Assess for Plasmodium parasites.
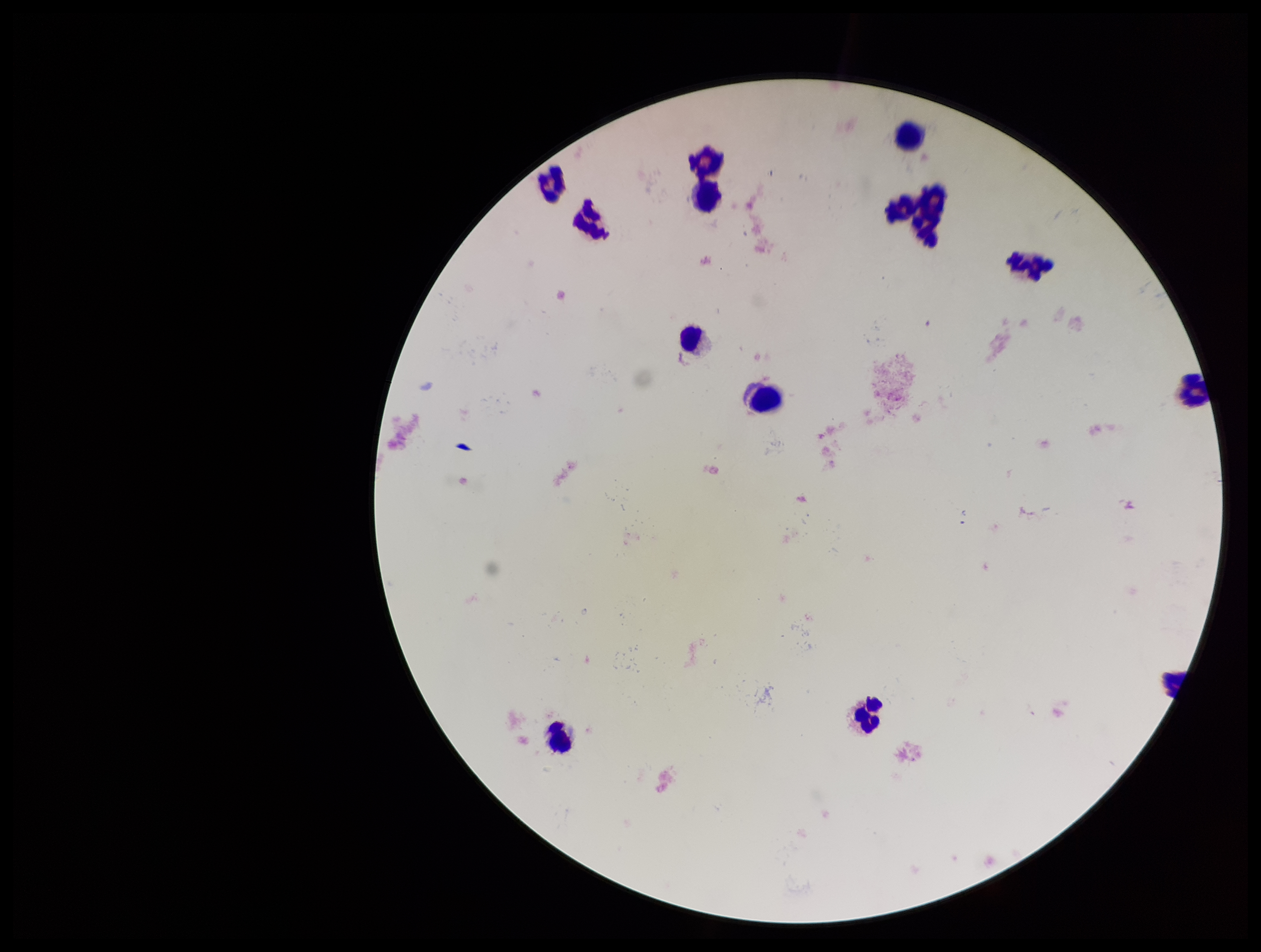

None identified.

Patient malaria status: negative. Single field of view. Parasite count: 0. Smartphone photograph taken through the eyepiece of a microscope. Stained with Giemsa. Preparation: thick smear. Leukocyte count: 14. Image is 1261×952 pixels.